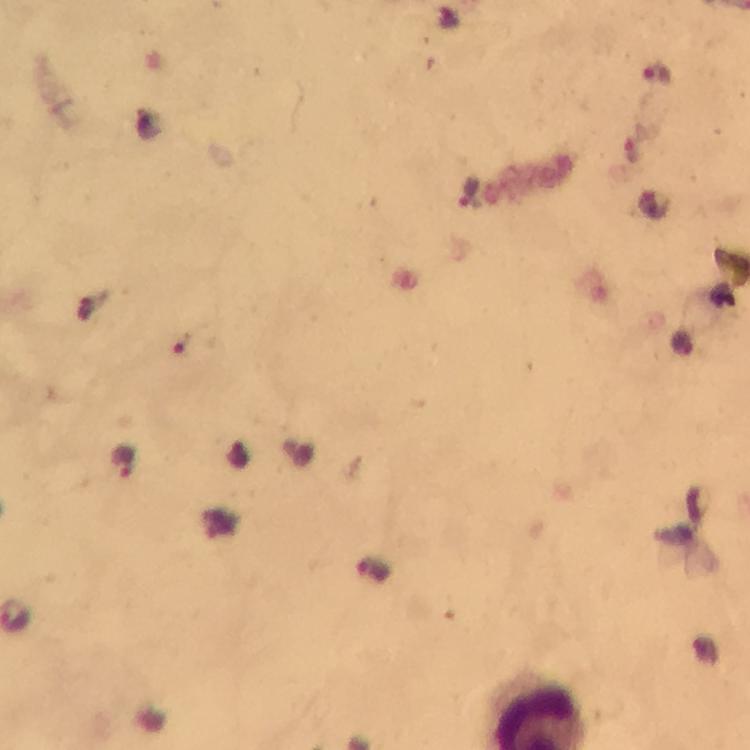

Approximate object centers, in pixels from the top-left corner. Malaria parasite locations: (x=659, y=73), (x=125, y=462). Immersion oil was used. Image is 750×750 pixels. A crop from one field of view. Smartphone photograph taken through a microscope. From a malaria diagnostic workup. 100x magnification. Thick blood film. Giemsa stain.